Classify this cell by malaria status.
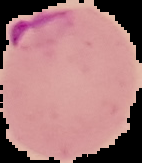

Parasitized.

Image is 142×163 pixels. Cell region segmented out of the field of view; the surrounding area is masked to black. From a thin blood film.